Identify the blood parasite species.
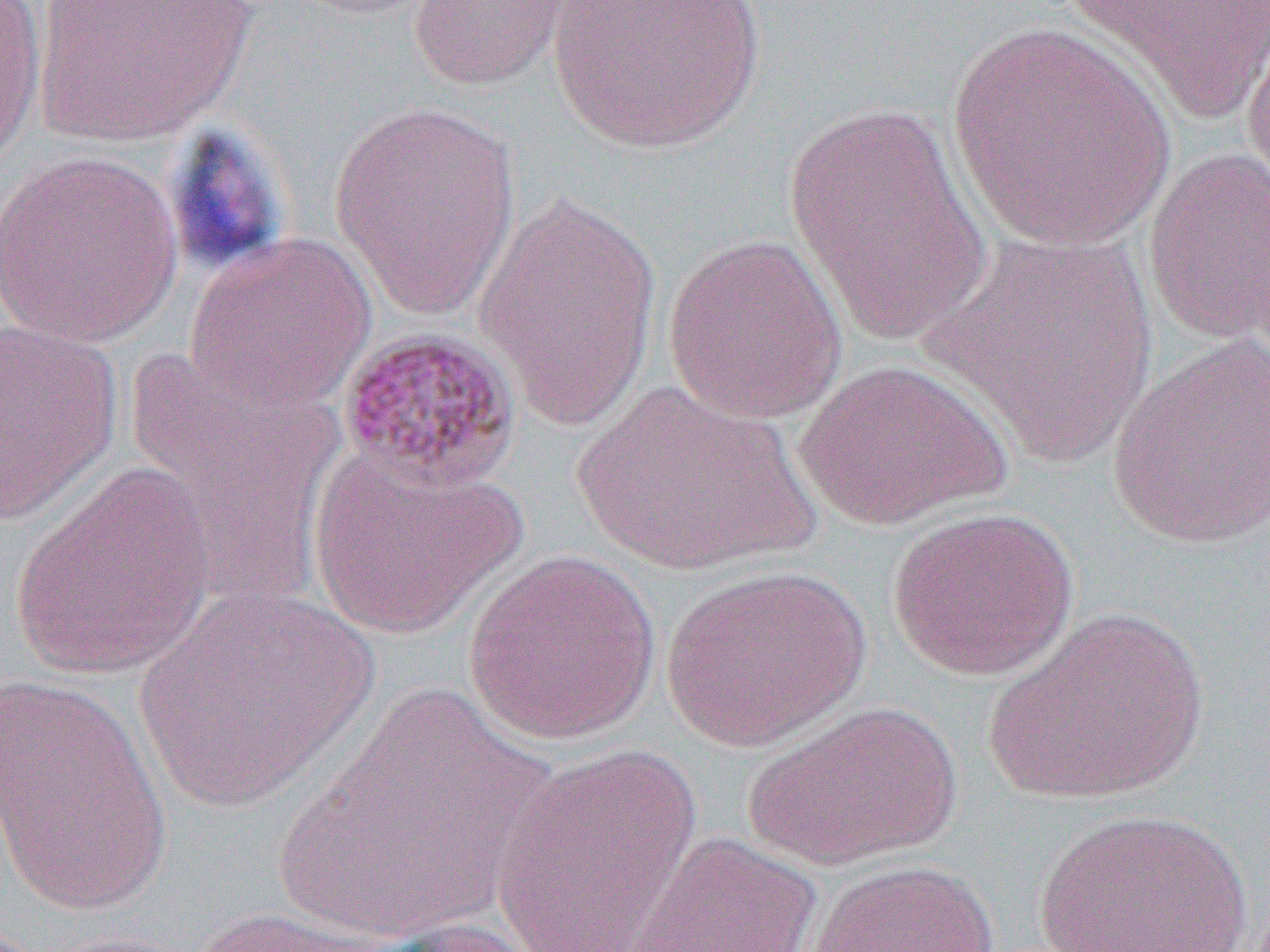

Plasmodium malariae.

Summary:
  - Coordinate format: approximate bounding boxes as (x1, y1, x2, y2) in pixels
  - Platelet locations: (160, 125, 294, 278)
  - Uninfected red blood cell locations: (0, 0, 47, 171), (30, 0, 257, 147), (406, 0, 583, 92), (544, 0, 770, 157), (1060, 0, 1269, 126), (1239, 11, 1270, 212), (946, 20, 1174, 252), (329, 98, 524, 319), (784, 104, 995, 347), (1141, 147, 1270, 346), (0, 148, 185, 349), (471, 190, 662, 429), (920, 229, 1160, 469), (185, 232, 377, 414), (663, 234, 848, 424), (0, 317, 123, 527), (1106, 334, 1270, 550), (122, 349, 347, 606), (792, 358, 1015, 531), (569, 380, 820, 577), (306, 446, 525, 639), (10, 464, 214, 681), (885, 506, 1079, 682), (462, 549, 662, 744), (660, 564, 872, 753), (130, 584, 379, 813), (985, 608, 1210, 807), (0, 672, 176, 915), (283, 679, 552, 950), (743, 700, 962, 869), (489, 743, 704, 951), (1034, 808, 1254, 952), (626, 831, 824, 952), (804, 859, 1001, 952), (180, 906, 410, 951), (360, 916, 551, 952)
  - Plasmodium malariae-infected red blood cell locations: (335, 324, 522, 494)
  - Image size: 1270×952 pixels
  - Modality: light microscopy
  - Magnification: 1000x
  - Preparation: thin blood film
  - Field of view: single